Assess for malaria.
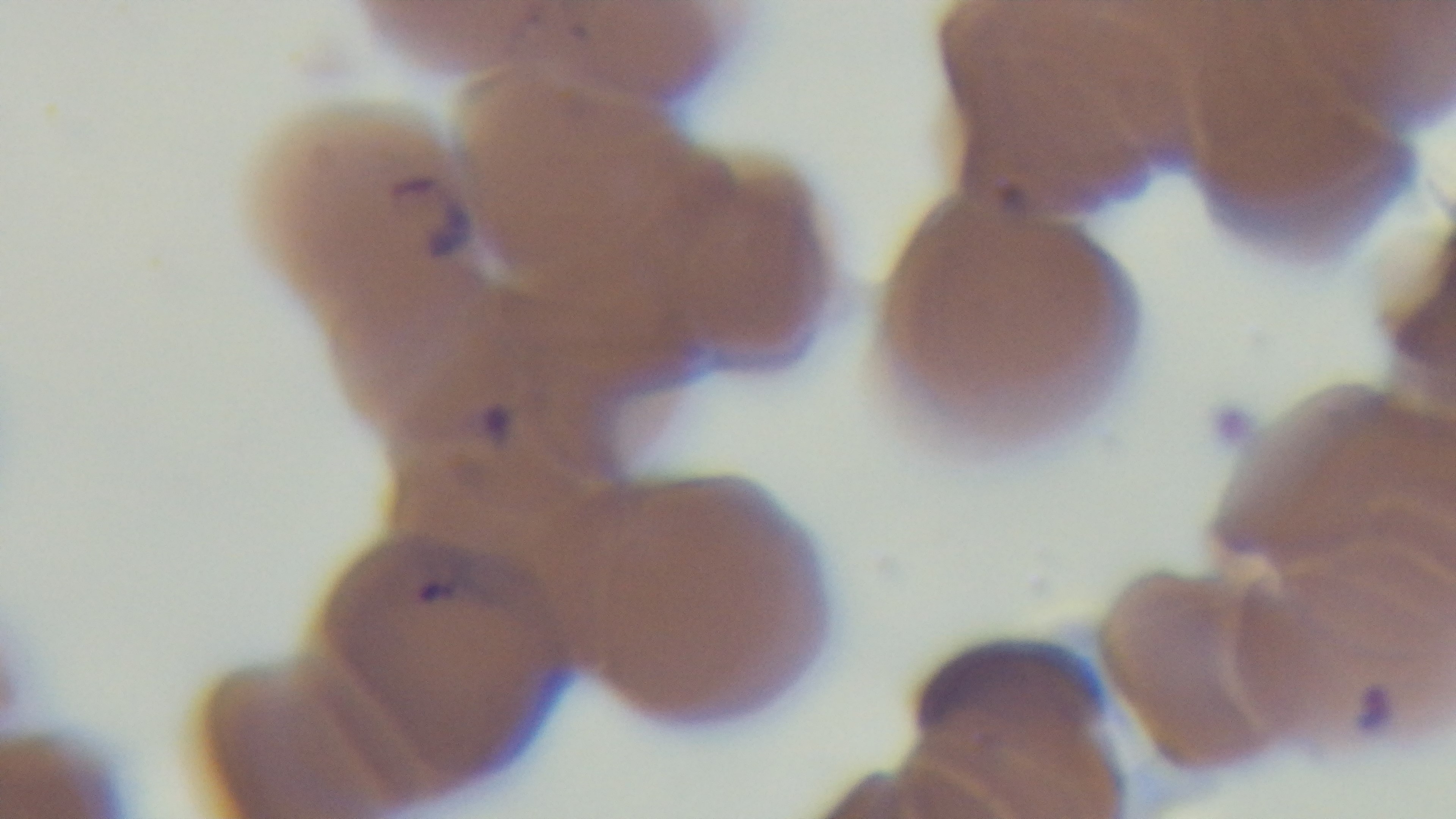
Positive.

{
  "field_of_view": "single",
  "capture": "mounted 4K digital camera",
  "preparation": "thin smear",
  "modality": "light microscopy",
  "stain": "Giemsa",
  "objective": "100x oil immersion"
}